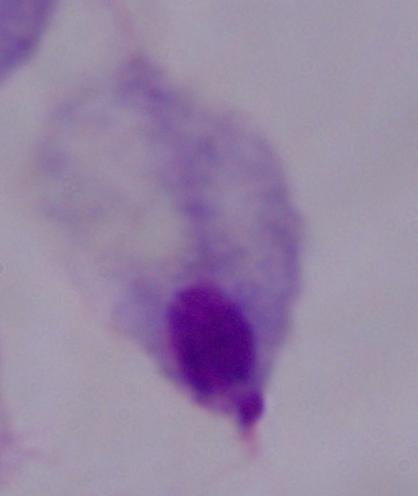

magnification = 1000x
identification = trichomonad
modality = micrograph